Classify this cell by malaria status.
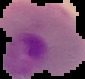

It is parasitized.

Summary:
  - Preparation: thin blood smear
  - Image type: segmented cell region with the area outside set to black
  - Image size: 85×79 pixels